Identify the parasite.
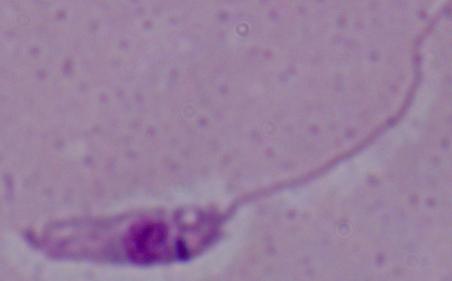

Leishmania.

Summary:
  - Modality: photomicrograph
  - Magnification: 1000x